Name the parasite shown.
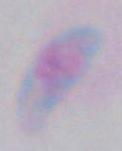
This is Toxoplasma gondii.

magnification = 1000x
modality = micrograph